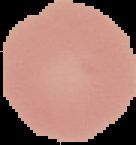
Summary:
  - Image type: segmented cell region with the area outside set to black
  - Malaria status: uninfected
  - Preparation: thin blood film
  - Image size: 136×145 pixels